Assess this cell for malaria.
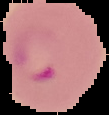

It is parasitized.

{
  "preparation": "thin blood film",
  "image_size": "109×115 pixels",
  "image_type": "segmented cell region on a black background"
}